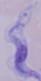

Summary:
  - Magnification: 1000x
  - Identification: trypanosome
  - Modality: photomicrograph